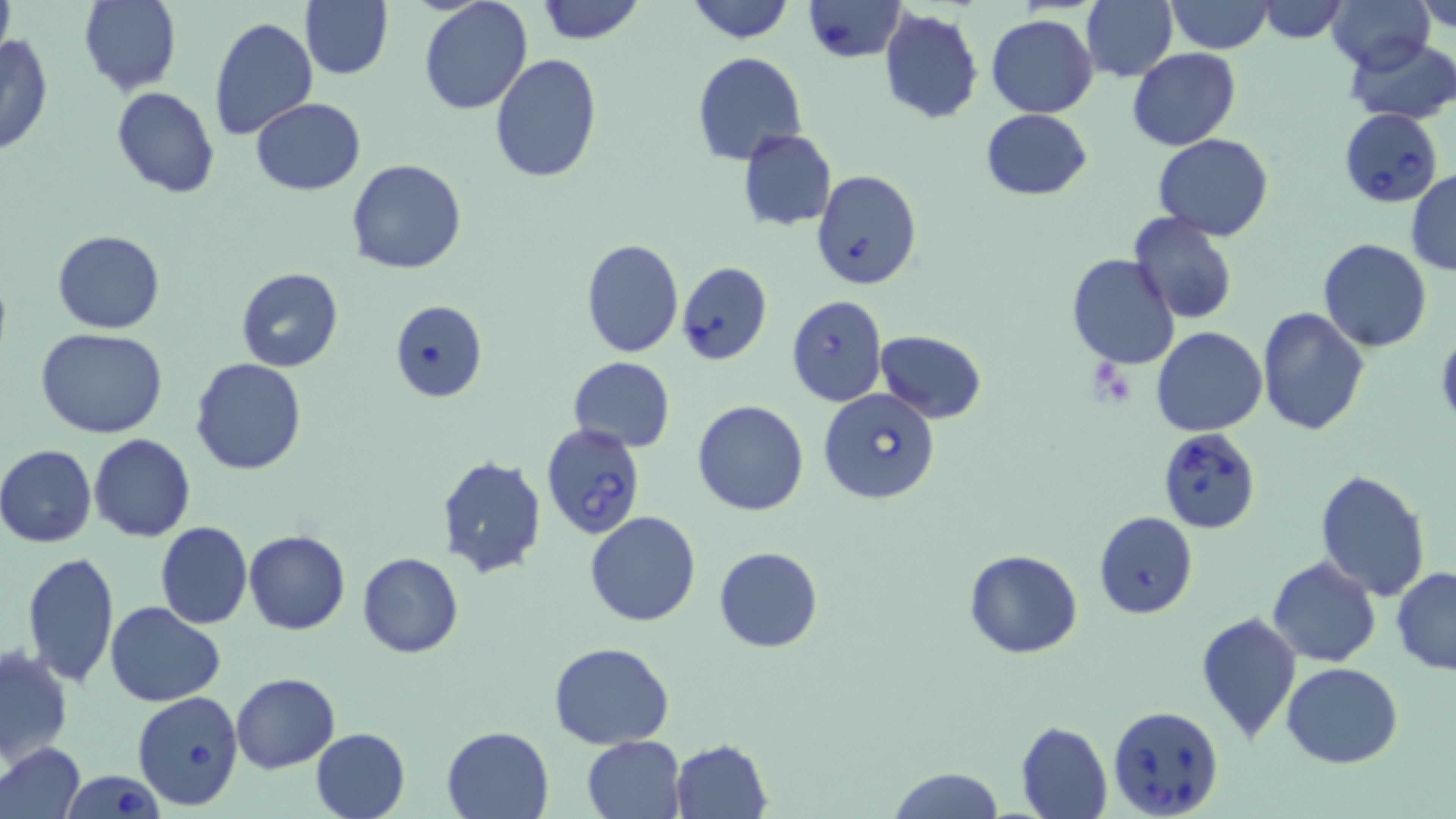

Approximate bounding boxes as (x1,y1)-(x2,y2) corner pairs in pixels. Uninfected red blood cell locations: (78,0)-(181,94), (301,0)-(392,81), (684,0)-(795,44), (1082,0)-(1178,83), (1165,0)-(1274,53), (1327,0)-(1436,72), (420,1)-(532,115), (533,1)-(648,46), (1415,1)-(1456,33), (0,2)-(14,59), (1256,2)-(1349,45), (878,7)-(984,124), (209,14)-(318,140), (986,14)-(1097,118), (0,33)-(53,157), (1345,36)-(1456,125), (1127,48)-(1241,150), (692,51)-(808,167), (490,55)-(602,184), (112,86)-(220,199), (249,98)-(366,195), (980,108)-(1093,200), (738,128)-(837,231), (1152,133)-(1274,239), (346,159)-(467,274), (1406,169)-(1456,273), (811,170)-(923,292), (1127,211)-(1237,323), (51,229)-(165,334), (1318,238)-(1432,352), (580,239)-(684,358), (1066,253)-(1180,371), (676,261)-(772,366), (235,267)-(342,371), (388,300)-(489,402), (1257,305)-(1370,436), (1150,325)-(1267,437), (36,326)-(169,439), (874,329)-(986,422), (568,356)-(675,452), (190,358)-(307,475), (691,399)-(810,516), (89,434)-(195,541), (0,446)-(97,549), (434,454)-(548,578), (1314,467)-(1431,600), (585,511)-(702,627), (1093,511)-(1199,620), (155,521)-(251,630), (244,530)-(351,634), (713,545)-(823,653), (963,549)-(1083,659), (22,550)-(120,689), (357,553)-(465,658), (1267,556)-(1382,668), (1393,566)-(1456,674), (106,602)-(227,707), (1195,610)-(1302,742), (549,641)-(675,748), (0,645)-(72,769), (1282,662)-(1404,767), (232,673)-(340,772), (1016,720)-(1113,819), (441,726)-(552,817), (310,728)-(410,819), (583,735)-(686,818), (667,739)-(774,819), (0,741)-(85,819), (888,767)-(1004,819). Babesia divergens-infected red blood cell locations: (802,0)-(906,62), (1338,108)-(1444,208), (786,294)-(888,406), (818,387)-(940,503), (539,423)-(645,544), (1158,427)-(1260,533), (132,692)-(247,810), (1107,705)-(1225,818), (61,770)-(166,818). Slide-level diagnosis: Babesia divergens. Image is 1456×819 pixels. Thin blood film. May-Grünwald-Giemsa-stained preparation. 1000x magnification. Light microscopy. One field of a larger specimen.